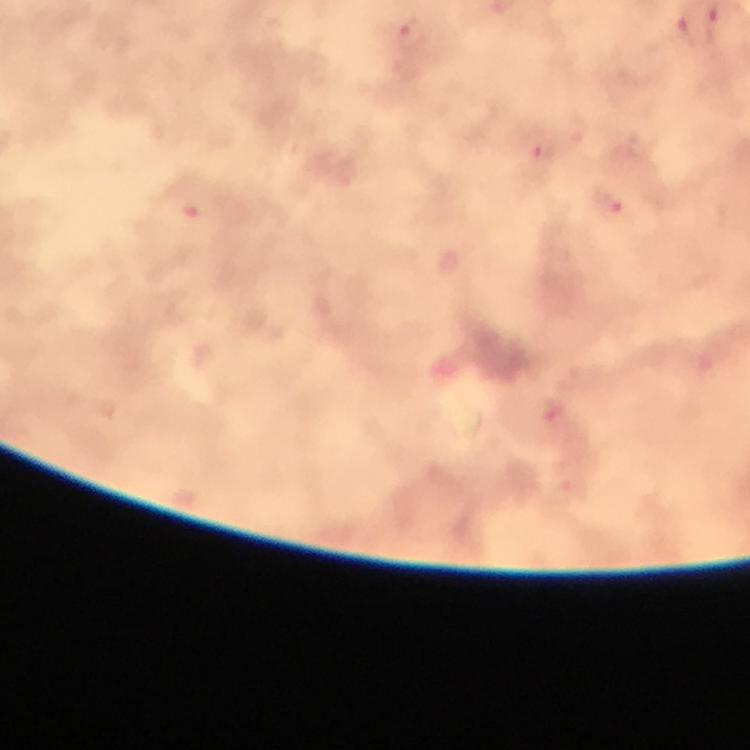
{
  "immersion_oil": "used",
  "capture": "smartphone mounted on the microscope",
  "cropped_from": "a single field of view",
  "context": "from a malaria diagnostic workup",
  "malaria_parasite_locations": "approximate centers as {x, y} in pixels: {715, 28}, {683, 30}, {414, 35}, {541, 153}, {608, 208}",
  "image_size": "750×750 pixels",
  "preparation": "thick smear",
  "stain": "Giemsa",
  "magnification": "100x"
}